Give the extent of all Plasmodium falciparum-infected red blood cells.
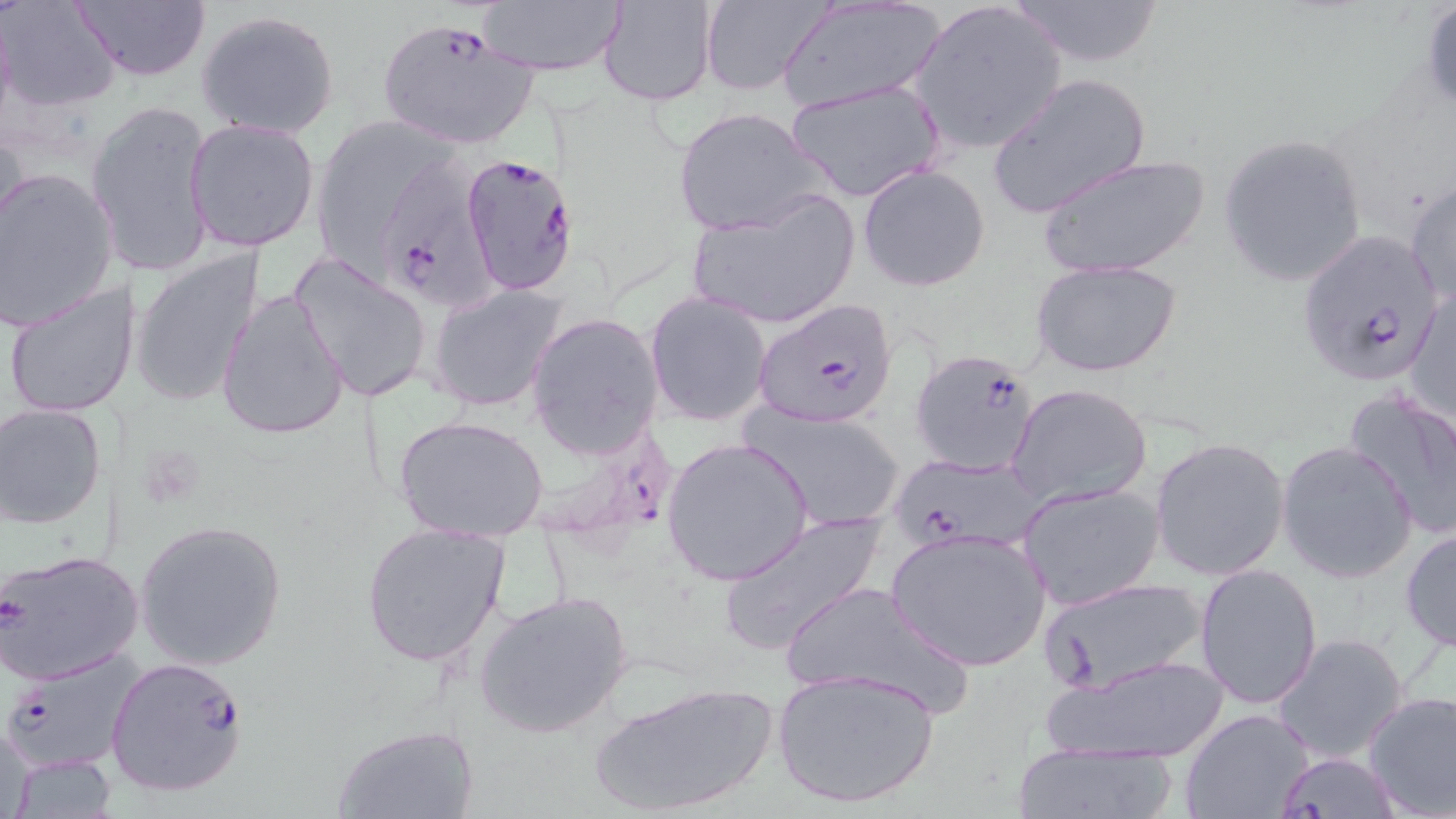

Approximate bounding boxes as named x1/y1/x2/y2 corners in pixels.
Plasmodium falciparum-infected red blood cells: (x1=377, y1=18, x2=540, y2=152), (x1=458, y1=153, x2=581, y2=292), (x1=382, y1=157, x2=497, y2=314), (x1=1296, y1=230, x2=1445, y2=390), (x1=754, y1=296, x2=898, y2=431), (x1=908, y1=346, x2=1043, y2=479), (x1=892, y1=451, x2=1045, y2=552), (x1=1, y1=547, x2=144, y2=685), (x1=3, y1=647, x2=144, y2=774), (x1=105, y1=655, x2=252, y2=799), (x1=1273, y1=752, x2=1401, y2=817).

Summary:
  - Uninfected red blood cell locations: (x1=2, y1=0, x2=121, y2=110), (x1=69, y1=0, x2=210, y2=82), (x1=477, y1=0, x2=625, y2=77), (x1=598, y1=0, x2=718, y2=107), (x1=698, y1=0, x2=831, y2=96), (x1=908, y1=0, x2=1068, y2=155), (x1=1003, y1=0, x2=1170, y2=69), (x1=1420, y1=1, x2=1456, y2=116), (x1=778, y1=3, x2=946, y2=109), (x1=196, y1=9, x2=341, y2=139), (x1=987, y1=72, x2=1150, y2=220), (x1=786, y1=78, x2=945, y2=204), (x1=87, y1=99, x2=216, y2=280), (x1=673, y1=106, x2=833, y2=236), (x1=185, y1=118, x2=320, y2=253), (x1=315, y1=119, x2=437, y2=276), (x1=1218, y1=132, x2=1368, y2=288), (x1=1039, y1=152, x2=1209, y2=281), (x1=858, y1=164, x2=991, y2=292), (x1=1, y1=168, x2=120, y2=330), (x1=1406, y1=178, x2=1455, y2=308), (x1=685, y1=188, x2=861, y2=331), (x1=131, y1=249, x2=265, y2=410), (x1=288, y1=251, x2=435, y2=405), (x1=1032, y1=258, x2=1182, y2=378), (x1=3, y1=280, x2=133, y2=419), (x1=428, y1=283, x2=567, y2=412), (x1=1406, y1=284, x2=1455, y2=428), (x1=216, y1=289, x2=350, y2=439), (x1=645, y1=291, x2=772, y2=428), (x1=526, y1=311, x2=664, y2=459), (x1=1008, y1=383, x2=1153, y2=507), (x1=1343, y1=387, x2=1456, y2=540), (x1=0, y1=403, x2=108, y2=529), (x1=744, y1=406, x2=907, y2=534), (x1=394, y1=414, x2=550, y2=540), (x1=1150, y1=435, x2=1293, y2=582), (x1=661, y1=437, x2=812, y2=586), (x1=1277, y1=441, x2=1418, y2=583), (x1=1016, y1=481, x2=1165, y2=612), (x1=718, y1=509, x2=886, y2=656), (x1=134, y1=521, x2=287, y2=671), (x1=1400, y1=523, x2=1456, y2=655), (x1=359, y1=524, x2=513, y2=668), (x1=885, y1=529, x2=1052, y2=673), (x1=1195, y1=563, x2=1325, y2=710), (x1=1036, y1=575, x2=1210, y2=697), (x1=780, y1=578, x2=973, y2=717), (x1=475, y1=590, x2=634, y2=740), (x1=1271, y1=632, x2=1410, y2=766), (x1=1044, y1=653, x2=1229, y2=763), (x1=773, y1=667, x2=941, y2=810), (x1=590, y1=680, x2=777, y2=816), (x1=1363, y1=690, x2=1456, y2=817), (x1=1180, y1=708, x2=1315, y2=818), (x1=1, y1=720, x2=40, y2=818), (x1=331, y1=723, x2=480, y2=818), (x1=1013, y1=741, x2=1176, y2=819), (x1=4, y1=753, x2=119, y2=817)
  - Slide-level diagnosis: Plasmodium falciparum
  - Modality: light microscopy
  - Magnification: 1000x
  - Field of view: one of a larger specimen
  - Image size: 1456×819 pixels
  - Preparation: thin blood smear
  - Stain: May-Grünwald-Giemsa